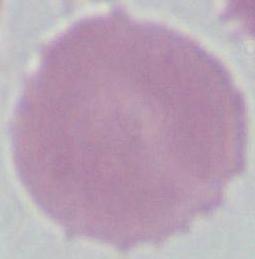

An erythrocyte is shown. Micrograph. 1000x magnification.